Give the position of every Plasmodium parasite.
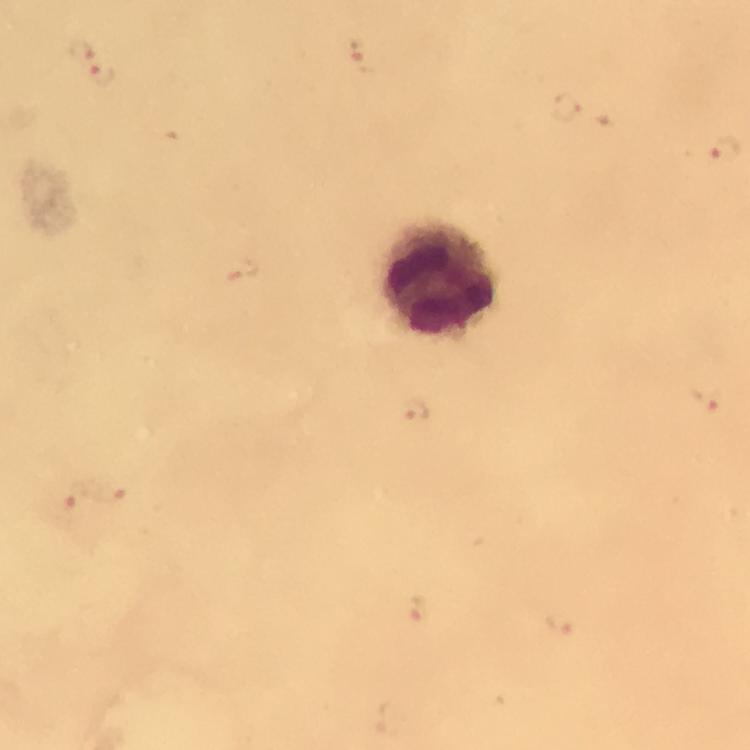

Approximate object centers, in pixels from the top-left corner.
Plasmodium parasites: (x=80, y=52), (x=362, y=55), (x=102, y=75), (x=568, y=107), (x=725, y=152), (x=706, y=399), (x=111, y=492), (x=70, y=499), (x=417, y=612), (x=562, y=624).

stain = Giemsa
image size = 750×750 pixels
immersion oil = used
magnification = 100x
context = from a diagnostic examination for malaria
capture = smartphone camera through the microscope
leukocyte locations = approximate object centers, in pixels from the top-left corner: (x=437, y=281)
preparation = thick smear
cropped from = a single field of view